State which parasite is depicted.
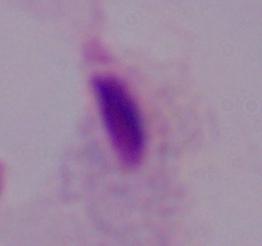

This is a trichomonad.

modality = micrograph
magnification = 1000x